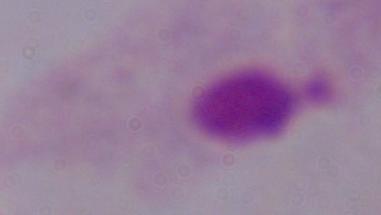

A trichomonad is seen. Photomicrograph. Captured at 1000x magnification.